Report the malaria status of this cell.
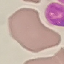

It is uninfected.

Summary:
  - Capture: smartphone through the microscope eyepiece
  - Image type: automatically extracted cell patch, resized to 64 × 64 pixels
  - Preparation: thin blood film
  - Stain: Giemsa